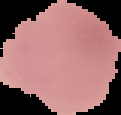

image type = segmented cell region on a black background
image size = 121×115 pixels
preparation = thin blood smear
malaria status = uninfected